Point out Plasmodium parasites and leukocytes.
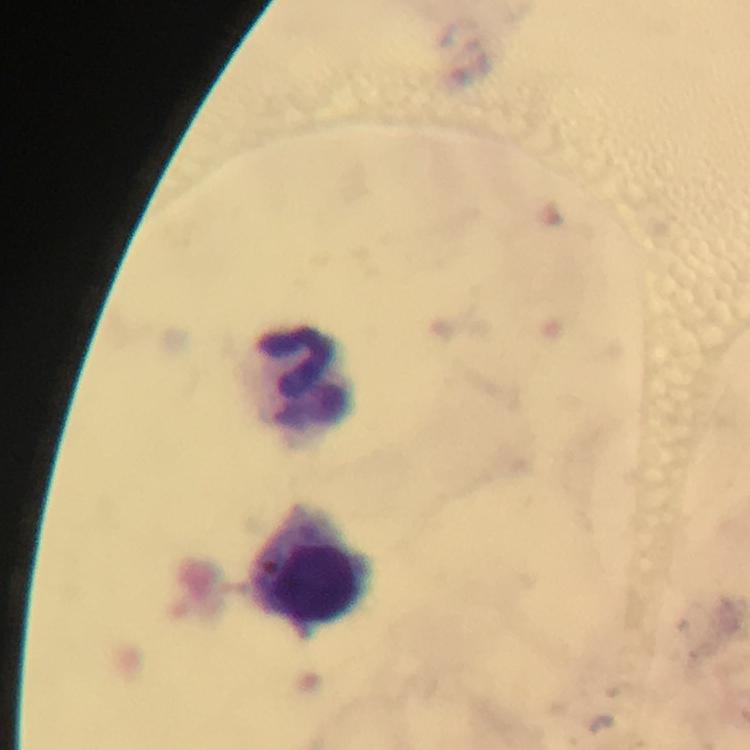

No Plasmodium parasites seen.
Approximate centers as [x, y] in pixels.
Leukocytes: [307, 380], [315, 567].

Summary:
  - Magnification: 100x
  - Context: from a malaria diagnostic workup
  - Preparation: thick blood film
  - Immersion oil: applied
  - Cropped from: a single field of view
  - Capture: smartphone photograph through a microscope
  - Image size: 750×750 pixels
  - Stain: Giemsa